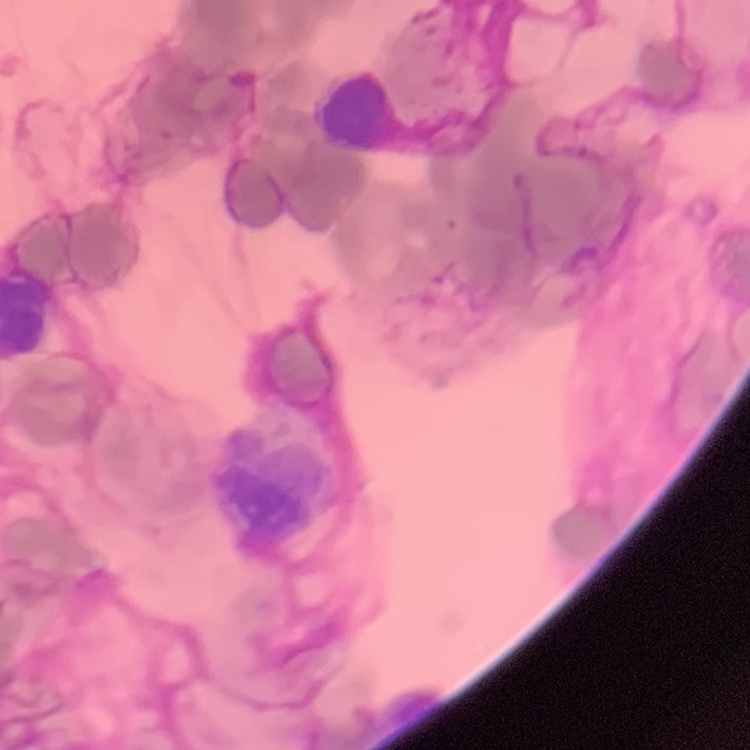

The red blood cells show rouleaux formation. Thin blood smear. One tile cut from a larger photomicrograph. Field's or Giemsa stain.